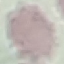
malaria status = uninfected
image type = cell patch, automatically extracted from a larger field of view and resized to 64 × 64 pixels
preparation = thin blood smear
capture = smartphone camera at the microscope eyepiece
stain = Giemsa